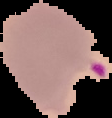

image size = 112×118 pixels
result = Plasmodium parasites identified
preparation = thin blood smear
image type = segmented cell region on a black background